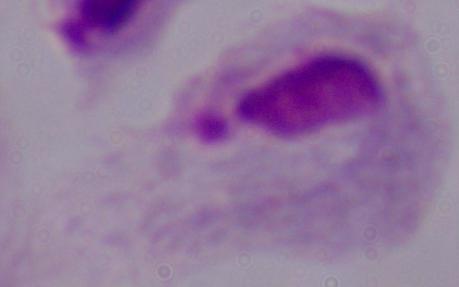 A trichomonad is seen. Captured at 1000x magnification. Photomicrograph.